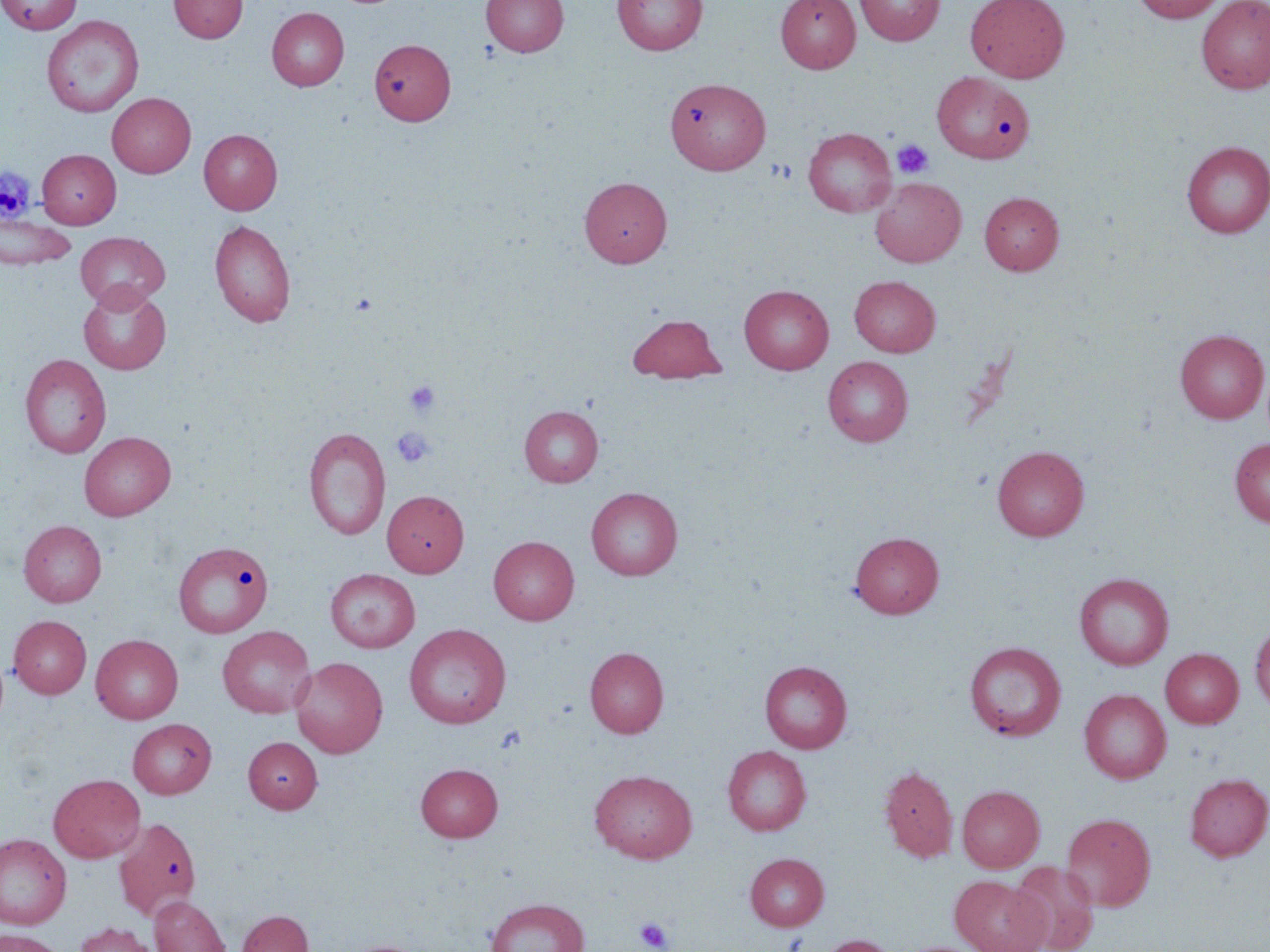

Approximate bounding boxes as named x1/y1/x2/y2 corners in pixels. Platelet locations: (x1=892, y1=139, x2=934, y2=179), (x1=404, y1=379, x2=440, y2=418), (x1=391, y1=427, x2=435, y2=467), (x1=634, y1=916, x2=674, y2=952). Uninfected red blood cell locations: (x1=0, y1=0, x2=82, y2=34), (x1=169, y1=0, x2=248, y2=43), (x1=481, y1=0, x2=569, y2=57), (x1=613, y1=0, x2=707, y2=55), (x1=775, y1=0, x2=860, y2=72), (x1=854, y1=0, x2=945, y2=45), (x1=965, y1=0, x2=1070, y2=82), (x1=1133, y1=0, x2=1225, y2=23), (x1=1196, y1=0, x2=1270, y2=94), (x1=266, y1=7, x2=349, y2=91), (x1=41, y1=16, x2=144, y2=118), (x1=370, y1=40, x2=456, y2=126), (x1=932, y1=71, x2=1033, y2=163), (x1=665, y1=76, x2=770, y2=175), (x1=107, y1=93, x2=196, y2=177), (x1=803, y1=127, x2=896, y2=217), (x1=199, y1=129, x2=282, y2=214), (x1=1181, y1=141, x2=1270, y2=238), (x1=37, y1=149, x2=121, y2=228), (x1=580, y1=177, x2=672, y2=267), (x1=870, y1=177, x2=966, y2=267), (x1=979, y1=191, x2=1064, y2=275), (x1=0, y1=214, x2=76, y2=270), (x1=209, y1=219, x2=296, y2=327), (x1=75, y1=231, x2=170, y2=311), (x1=849, y1=275, x2=941, y2=357), (x1=79, y1=285, x2=171, y2=375), (x1=739, y1=285, x2=834, y2=374), (x1=627, y1=313, x2=726, y2=383), (x1=1176, y1=330, x2=1269, y2=423), (x1=20, y1=354, x2=111, y2=458), (x1=823, y1=356, x2=913, y2=446), (x1=519, y1=405, x2=603, y2=487), (x1=303, y1=426, x2=390, y2=541), (x1=78, y1=432, x2=175, y2=519), (x1=1230, y1=438, x2=1270, y2=528), (x1=993, y1=445, x2=1090, y2=541), (x1=586, y1=487, x2=683, y2=580), (x1=382, y1=490, x2=469, y2=577), (x1=19, y1=520, x2=107, y2=606), (x1=850, y1=531, x2=944, y2=618), (x1=488, y1=536, x2=579, y2=625), (x1=173, y1=540, x2=274, y2=638), (x1=325, y1=568, x2=420, y2=652), (x1=1074, y1=572, x2=1174, y2=670), (x1=9, y1=615, x2=92, y2=698), (x1=1250, y1=621, x2=1270, y2=712), (x1=404, y1=624, x2=511, y2=728), (x1=217, y1=625, x2=316, y2=718), (x1=91, y1=634, x2=183, y2=724), (x1=964, y1=641, x2=1066, y2=741), (x1=585, y1=647, x2=669, y2=737), (x1=1160, y1=648, x2=1243, y2=728), (x1=290, y1=656, x2=388, y2=757), (x1=759, y1=660, x2=852, y2=753), (x1=1079, y1=688, x2=1171, y2=783), (x1=127, y1=718, x2=216, y2=799), (x1=243, y1=737, x2=323, y2=813), (x1=723, y1=745, x2=811, y2=835), (x1=415, y1=763, x2=503, y2=842), (x1=879, y1=765, x2=958, y2=862), (x1=589, y1=769, x2=697, y2=863), (x1=1184, y1=773, x2=1270, y2=861), (x1=48, y1=774, x2=146, y2=862), (x1=957, y1=785, x2=1044, y2=872), (x1=1061, y1=812, x2=1156, y2=911), (x1=113, y1=817, x2=202, y2=920), (x1=0, y1=833, x2=72, y2=929), (x1=745, y1=852, x2=828, y2=931), (x1=1009, y1=861, x2=1100, y2=952), (x1=950, y1=875, x2=1049, y2=952), (x1=149, y1=896, x2=231, y2=952), (x1=485, y1=898, x2=589, y2=952), (x1=237, y1=910, x2=314, y2=952), (x1=73, y1=922, x2=160, y2=952), (x1=0, y1=929, x2=66, y2=952), (x1=818, y1=934, x2=899, y2=952), (x1=340, y1=939, x2=433, y2=952). Slide-level diagnosis: no evidence of blood parasites. One field of a larger specimen. Thin blood film. Light microscopy. Image is 1270×952 pixels. May-Grünwald-Giemsa stain. 1000x magnification.